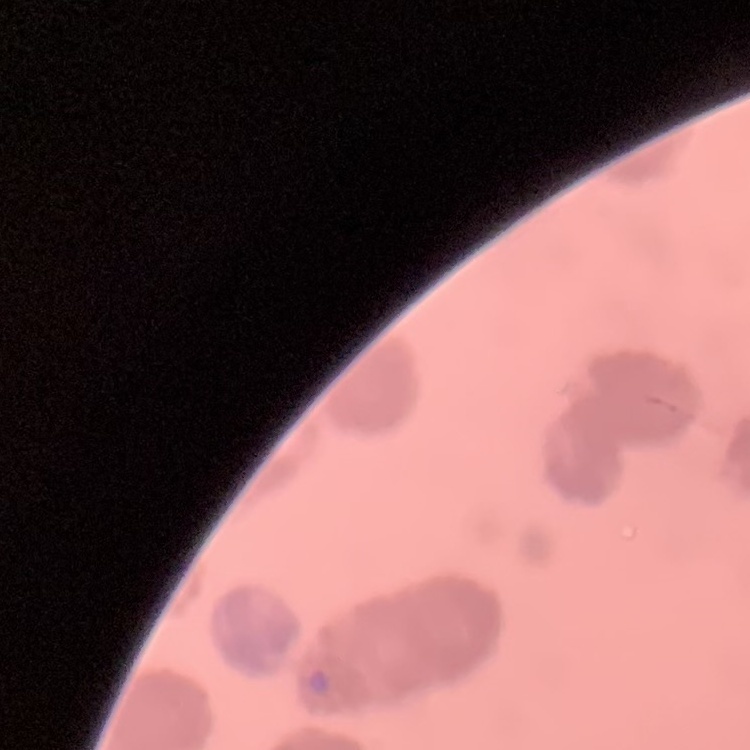
{
  "red_blood_cell_morphology": "rouleaux formation",
  "preparation": "thin peripheral smear",
  "image_type": "square crop of a larger photomicrograph",
  "stain": "Field's or Giemsa"
}